Identify the parasite.
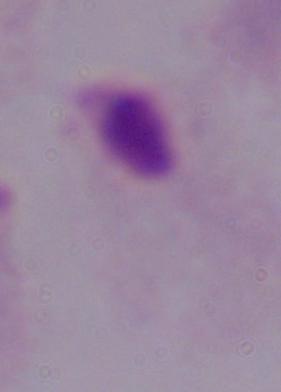
A trichomonad.

1000x magnification. Photomicrograph.